Classify this cell by malaria status.
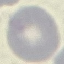
It is uninfected.

capture = smartphone through the microscope eyepiece
stain = Giemsa
image type = cell patch, automatically extracted from a larger field of view and resized to 64 × 64 pixels
preparation = thin smear